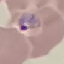

Summary:
  - Malaria status: parasitized
  - Preparation: thin blood film
  - Capture: smartphone through the microscope eyepiece
  - Stain: Giemsa
  - Image type: automatically extracted cell patch, resized to 64 × 64 pixels